Give the position of every leukocyte visible.
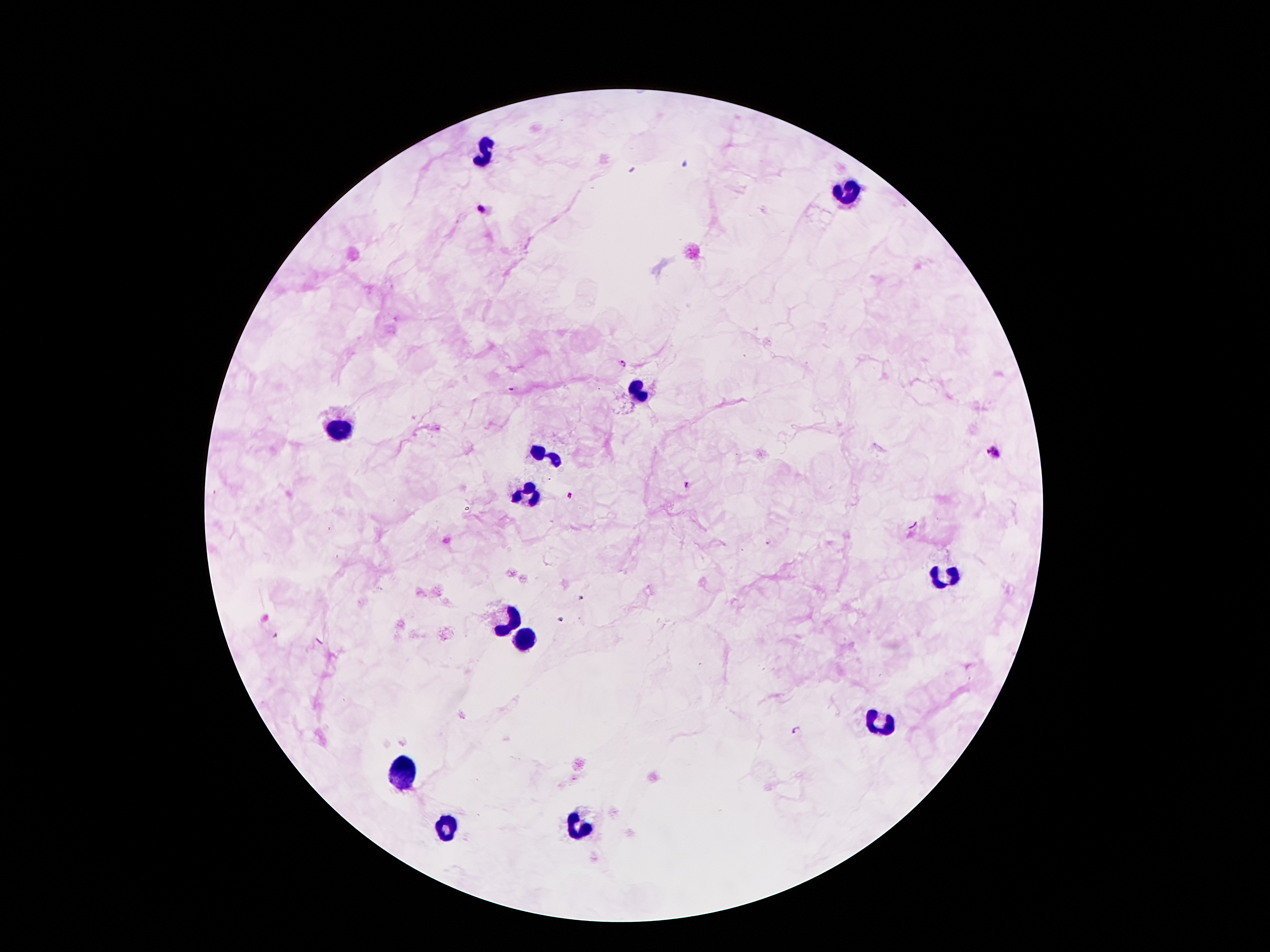

Approximate object centers, in pixels from the top-left corner.
Leukocytes: (x=485, y=153), (x=842, y=191), (x=636, y=391), (x=338, y=431), (x=543, y=455), (x=531, y=496), (x=946, y=578), (x=506, y=622), (x=527, y=637), (x=879, y=723), (x=407, y=774), (x=443, y=826), (x=575, y=831).

Summary:
  - Malaria parasite locations: (x=481, y=206), (x=623, y=365), (x=511, y=389), (x=992, y=452), (x=688, y=485), (x=571, y=497), (x=768, y=542), (x=796, y=730)
  - Preparation: thick blood smear
  - Stain: Giemsa
  - Magnification: 100x
  - Patient malaria status: positive for Plasmodium falciparum
  - Field of view: single
  - Capture: smartphone through the microscope eyepiece
  - Image size: 1270×952 pixels